Locate every blood parasite and identify its species.
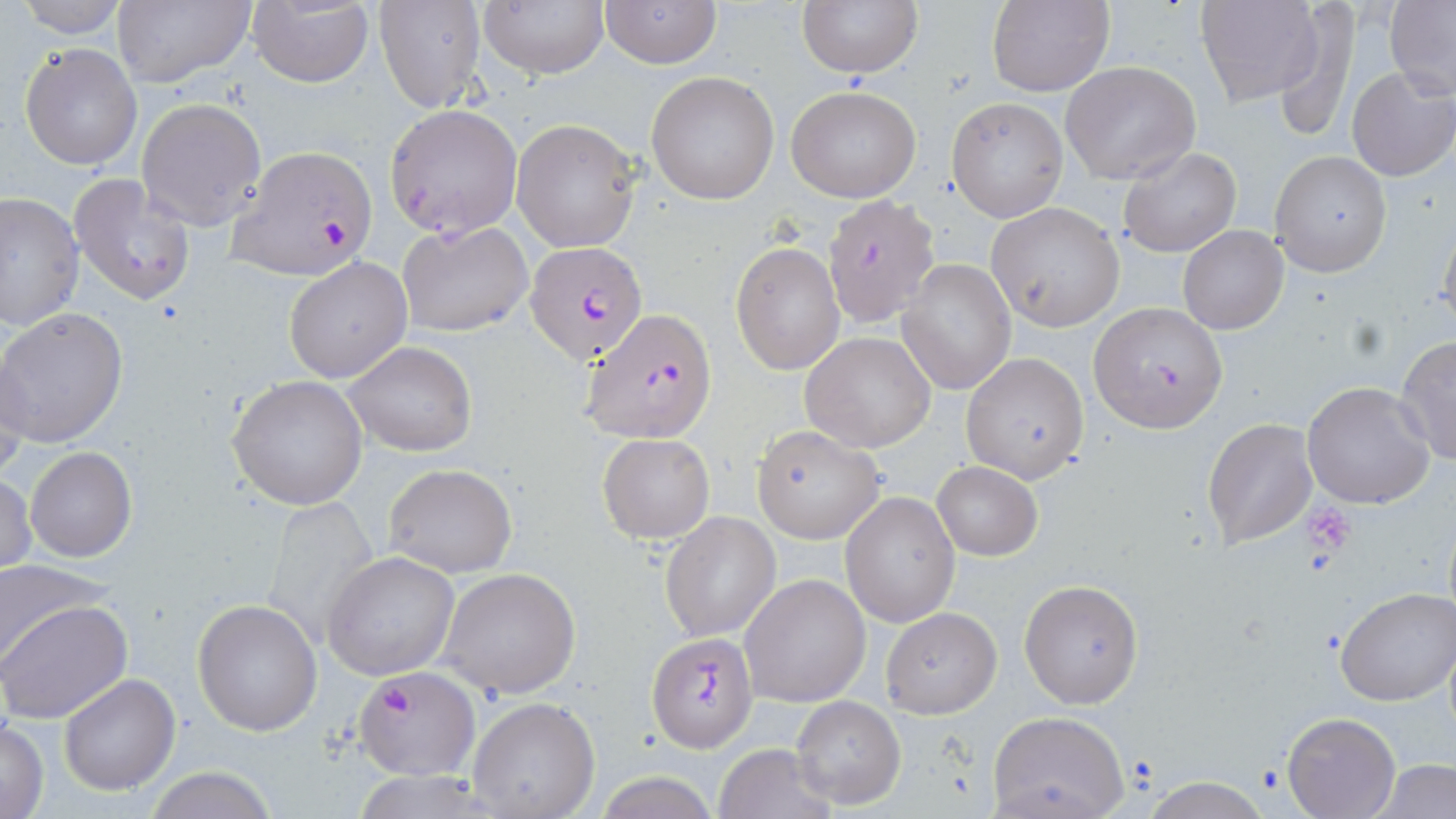
Approximate bounding boxes as (x1, y1, x2, y2) in pixels.
Plasmodium falciparum-infected red blood cells: (228, 143, 378, 280), (527, 241, 648, 367), (581, 309, 718, 443), (648, 634, 758, 751), (354, 666, 478, 780).
No Plasmodium ovale, Plasmodium malariae, Plasmodium vivax, Babesia divergens, or Trypanosoma brucei observed.

Summary:
  - Uninfected red blood cell locations: (12, 0, 130, 40), (375, 0, 486, 113), (599, 0, 722, 69), (797, 0, 922, 78), (987, 0, 1113, 97), (1196, 0, 1323, 107), (1272, 0, 1363, 142), (111, 1, 255, 88), (246, 1, 376, 88), (476, 1, 609, 78), (1385, 1, 1456, 100), (19, 42, 143, 171), (1061, 61, 1201, 185), (1345, 66, 1456, 181), (646, 71, 780, 205), (786, 86, 921, 203), (138, 97, 268, 230), (946, 97, 1066, 221), (384, 103, 524, 238), (511, 118, 642, 254), (1118, 146, 1240, 257), (1269, 150, 1392, 276), (68, 174, 196, 305), (0, 190, 84, 329), (820, 195, 943, 330), (988, 204, 1123, 330), (1437, 214, 1456, 335), (396, 219, 532, 338), (1178, 224, 1288, 335), (731, 241, 844, 375), (284, 257, 412, 383), (895, 258, 1016, 395), (1087, 301, 1228, 433), (0, 307, 129, 448), (799, 331, 936, 454), (1395, 337, 1456, 466), (342, 341, 476, 457), (0, 348, 31, 479), (960, 352, 1090, 484), (227, 374, 368, 511), (1303, 382, 1436, 508), (1202, 418, 1318, 549), (752, 424, 885, 543), (598, 432, 714, 543), (24, 447, 136, 562), (932, 461, 1042, 561), (383, 463, 517, 577), (1, 473, 37, 576), (840, 492, 961, 628), (260, 494, 377, 650), (661, 513, 781, 641), (322, 552, 461, 681), (0, 560, 105, 669), (438, 567, 581, 699), (740, 573, 872, 707), (1020, 579, 1144, 708), (1334, 585, 1455, 706), (1, 596, 131, 724), (192, 598, 323, 737), (880, 606, 1002, 719), (58, 674, 181, 793), (790, 695, 906, 808), (467, 696, 601, 819), (988, 711, 1131, 819), (1282, 712, 1400, 818), (1, 716, 50, 819), (713, 743, 836, 819), (1374, 757, 1456, 817), (139, 766, 279, 819), (592, 772, 723, 819), (1142, 779, 1270, 817)
  - Platelet locations: (1304, 506, 1357, 556)
  - Slide-level diagnosis: Plasmodium falciparum
  - Field of view: single
  - Magnification: 1000x
  - Modality: optical microscopy
  - Stain: May-Grünwald-Giemsa
  - Preparation: thin blood film
  - Image size: 1456×819 pixels